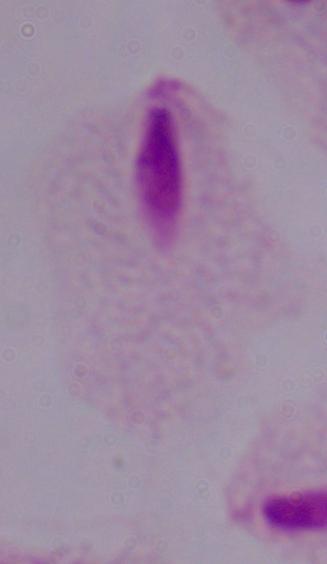
Summary:
  - Magnification: 1000x
  - Modality: photomicrograph
  - Identification: trichomonad